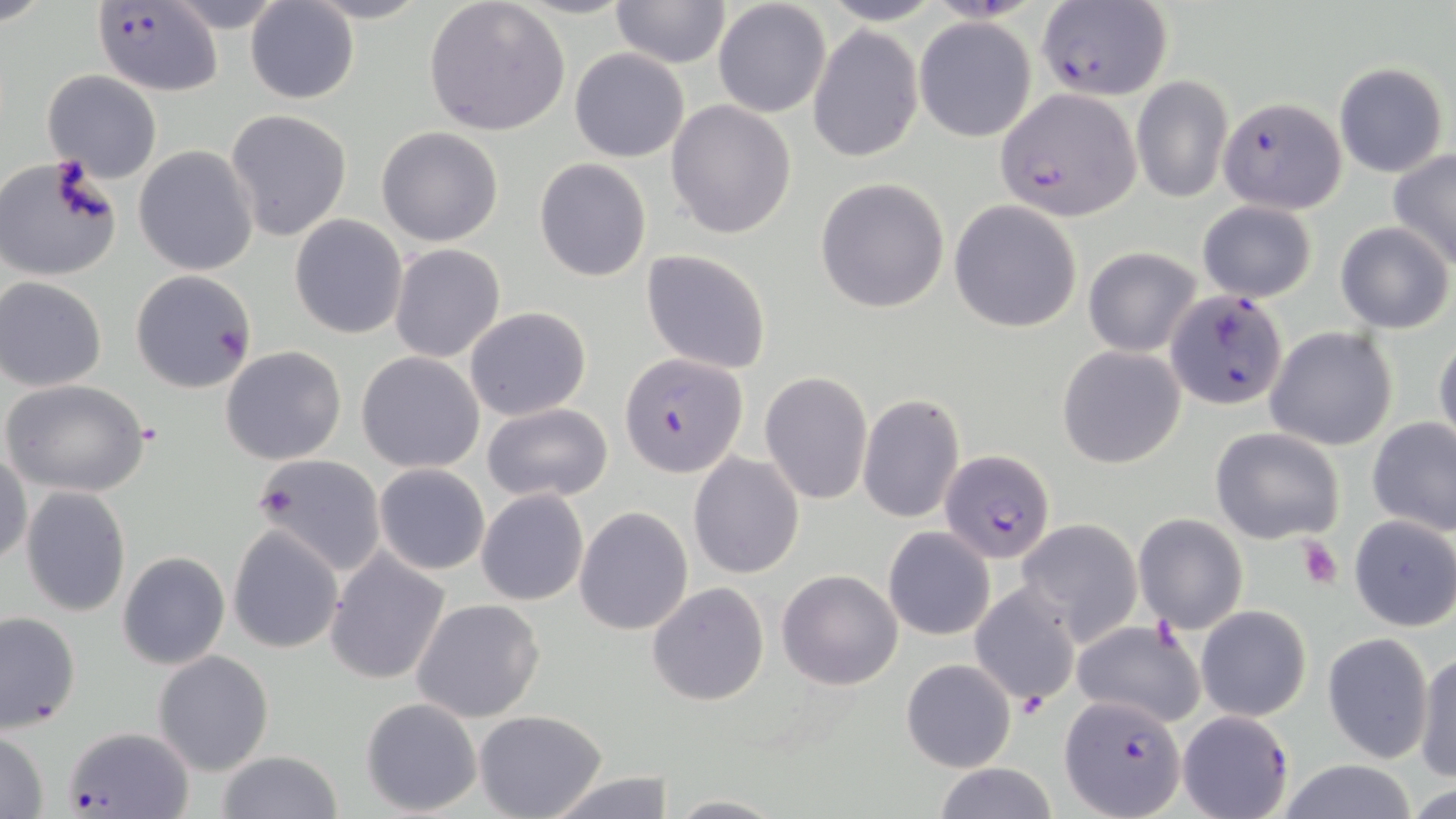
Summary:
  - Coordinate format: approximate bounding boxes as named x1/y1/x2/y2 corners in pixels
  - Uninfected red blood cell locations: (x1=161, y1=0, x2=292, y2=31), (x1=608, y1=0, x2=730, y2=68), (x1=423, y1=1, x2=570, y2=136), (x1=712, y1=1, x2=832, y2=118), (x1=245, y1=2, x2=359, y2=105), (x1=914, y1=17, x2=1036, y2=142), (x1=808, y1=26, x2=923, y2=162), (x1=569, y1=48, x2=689, y2=162), (x1=1332, y1=62, x2=1450, y2=177), (x1=43, y1=70, x2=162, y2=183), (x1=1131, y1=76, x2=1232, y2=204), (x1=666, y1=99, x2=798, y2=239), (x1=225, y1=109, x2=353, y2=243), (x1=375, y1=125, x2=505, y2=247), (x1=134, y1=146, x2=259, y2=276), (x1=1388, y1=148, x2=1456, y2=269), (x1=0, y1=154, x2=124, y2=282), (x1=534, y1=158, x2=651, y2=282), (x1=814, y1=177, x2=950, y2=313), (x1=1195, y1=199, x2=1318, y2=302), (x1=950, y1=200, x2=1082, y2=334), (x1=289, y1=215, x2=408, y2=340), (x1=1334, y1=222, x2=1454, y2=333), (x1=389, y1=243, x2=505, y2=362), (x1=1083, y1=247, x2=1201, y2=356), (x1=641, y1=249, x2=771, y2=374), (x1=129, y1=270, x2=258, y2=393), (x1=1, y1=278, x2=107, y2=391), (x1=465, y1=307, x2=592, y2=421), (x1=1266, y1=326, x2=1398, y2=452), (x1=1433, y1=334, x2=1456, y2=452), (x1=1056, y1=344, x2=1187, y2=468), (x1=220, y1=346, x2=346, y2=465), (x1=357, y1=351, x2=485, y2=472), (x1=759, y1=371, x2=872, y2=506), (x1=4, y1=380, x2=151, y2=497), (x1=857, y1=393, x2=965, y2=524), (x1=481, y1=401, x2=614, y2=505), (x1=1367, y1=417, x2=1456, y2=535), (x1=1211, y1=425, x2=1346, y2=545), (x1=0, y1=448, x2=31, y2=566), (x1=688, y1=453, x2=804, y2=579), (x1=253, y1=455, x2=387, y2=575), (x1=374, y1=464, x2=490, y2=575), (x1=20, y1=485, x2=131, y2=617), (x1=477, y1=489, x2=589, y2=606), (x1=575, y1=505, x2=692, y2=636), (x1=1132, y1=514, x2=1247, y2=634), (x1=1349, y1=515, x2=1456, y2=632), (x1=1017, y1=518, x2=1143, y2=645), (x1=227, y1=524, x2=344, y2=653), (x1=882, y1=525, x2=997, y2=641), (x1=325, y1=550, x2=452, y2=685), (x1=118, y1=551, x2=230, y2=671), (x1=777, y1=567, x2=904, y2=690), (x1=970, y1=582, x2=1081, y2=708), (x1=647, y1=583, x2=769, y2=707), (x1=411, y1=597, x2=546, y2=722), (x1=1196, y1=605, x2=1311, y2=721), (x1=0, y1=611, x2=81, y2=733), (x1=1070, y1=619, x2=1205, y2=728), (x1=1322, y1=633, x2=1433, y2=762), (x1=152, y1=649, x2=274, y2=775), (x1=1413, y1=650, x2=1456, y2=782), (x1=901, y1=658, x2=1016, y2=772), (x1=360, y1=697, x2=482, y2=817), (x1=474, y1=710, x2=608, y2=819), (x1=0, y1=731, x2=51, y2=818), (x1=214, y1=751, x2=343, y2=819), (x1=1271, y1=761, x2=1422, y2=819), (x1=931, y1=762, x2=1060, y2=819), (x1=541, y1=770, x2=676, y2=819), (x1=666, y1=795, x2=787, y2=818)
  - Plasmodium falciparum-infected red blood cell locations: (x1=1033, y1=2, x2=1172, y2=100), (x1=92, y1=5, x2=224, y2=96), (x1=998, y1=89, x2=1142, y2=219), (x1=1219, y1=95, x2=1346, y2=212), (x1=1164, y1=288, x2=1291, y2=412), (x1=621, y1=354, x2=746, y2=477), (x1=940, y1=448, x2=1055, y2=563), (x1=1060, y1=694, x2=1185, y2=818), (x1=1176, y1=708, x2=1295, y2=819), (x1=67, y1=725, x2=191, y2=817)
  - Platelet locations: (x1=256, y1=483, x2=303, y2=523), (x1=1295, y1=537, x2=1344, y2=589)
  - Slide-level diagnosis: Plasmodium falciparum
  - Modality: optical microscopy
  - Field of view: one of a larger specimen
  - Preparation: thin blood film
  - Image size: 1456×819 pixels
  - Stain: May-Grünwald-Giemsa
  - Magnification: 1000x